Assess this cell for malaria.
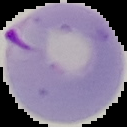
Parasitized.

image type = segmented cell region with the area outside set to black
image size = 127×127 pixels
preparation = thin blood smear